Give the extent of all Plasmodium falciparum-infected red blood cells.
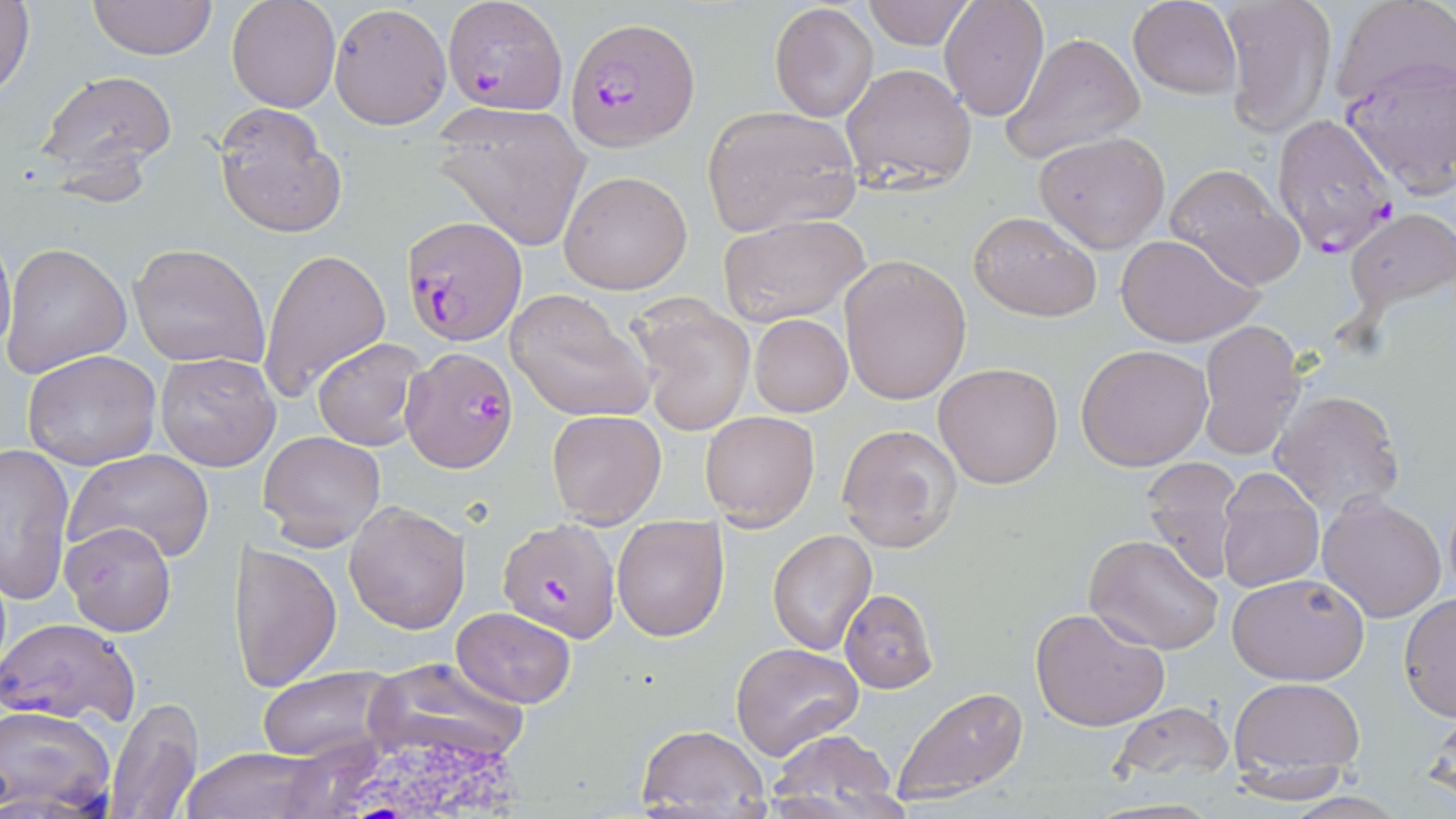
Approximate bounding boxes as (x1, y1, x2, y2) in pixels.
Plasmodium falciparum-infected red blood cells: (439, 0, 567, 112), (568, 18, 700, 150), (1271, 112, 1398, 259), (399, 215, 524, 346), (400, 346, 517, 472), (498, 518, 621, 642).

slide-level diagnosis = Plasmodium falciparum
field of view = single
image size = 1456×819 pixels
magnification = 1000x
white blood cell locations = approximate bounding boxes as (x1, y1, x2, y2) in pixels: (334, 730, 530, 819)
uninfected red blood cell locations = approximate bounding boxes as (x1, y1, x2, y2) in pixels: (87, 0, 219, 61), (227, 0, 340, 112), (861, 0, 978, 50), (939, 0, 1050, 121), (1126, 0, 1243, 97), (1221, 0, 1337, 138), (1332, 0, 1454, 109), (1, 1, 35, 101), (770, 2, 878, 122), (329, 5, 448, 127), (1000, 32, 1145, 163), (1339, 58, 1456, 196), (841, 62, 978, 193), (37, 69, 177, 182), (214, 103, 346, 236), (701, 106, 861, 235), (433, 107, 591, 249), (1034, 131, 1170, 251), (1164, 163, 1305, 288), (559, 170, 692, 295), (1344, 206, 1456, 318), (967, 210, 1101, 321), (717, 212, 871, 329), (0, 230, 15, 364), (1116, 234, 1261, 347), (1, 241, 131, 378), (129, 242, 269, 370), (257, 247, 391, 402), (839, 255, 971, 404), (506, 288, 656, 420), (627, 297, 757, 437), (749, 315, 853, 417), (1196, 320, 1307, 459), (311, 336, 427, 450), (1075, 344, 1213, 469), (22, 349, 162, 468), (154, 351, 280, 472), (933, 361, 1063, 488), (1269, 389, 1405, 518), (547, 409, 667, 526), (700, 409, 820, 528), (835, 423, 963, 553), (260, 428, 385, 552), (1, 444, 73, 605), (65, 448, 215, 566), (1140, 457, 1241, 583), (1216, 469, 1323, 593), (1318, 491, 1449, 623), (343, 499, 471, 633), (612, 517, 729, 641), (60, 521, 177, 637), (768, 529, 877, 654), (1085, 535, 1223, 653), (230, 543, 343, 691), (1226, 572, 1370, 685), (839, 589, 939, 693), (1399, 592, 1455, 720), (1029, 605, 1172, 734), (451, 606, 577, 708), (1, 616, 142, 729), (731, 641, 863, 760), (363, 656, 531, 766), (258, 665, 400, 763), (1229, 677, 1366, 788), (890, 684, 1030, 803), (105, 696, 203, 819), (1422, 698, 1456, 808), (1107, 699, 1239, 788), (0, 701, 116, 813), (634, 724, 771, 815), (767, 731, 905, 817), (177, 748, 336, 819)
stain = May-Grünwald-Giemsa
preparation = thin blood film
modality = light microscopy